Assess the background quality.
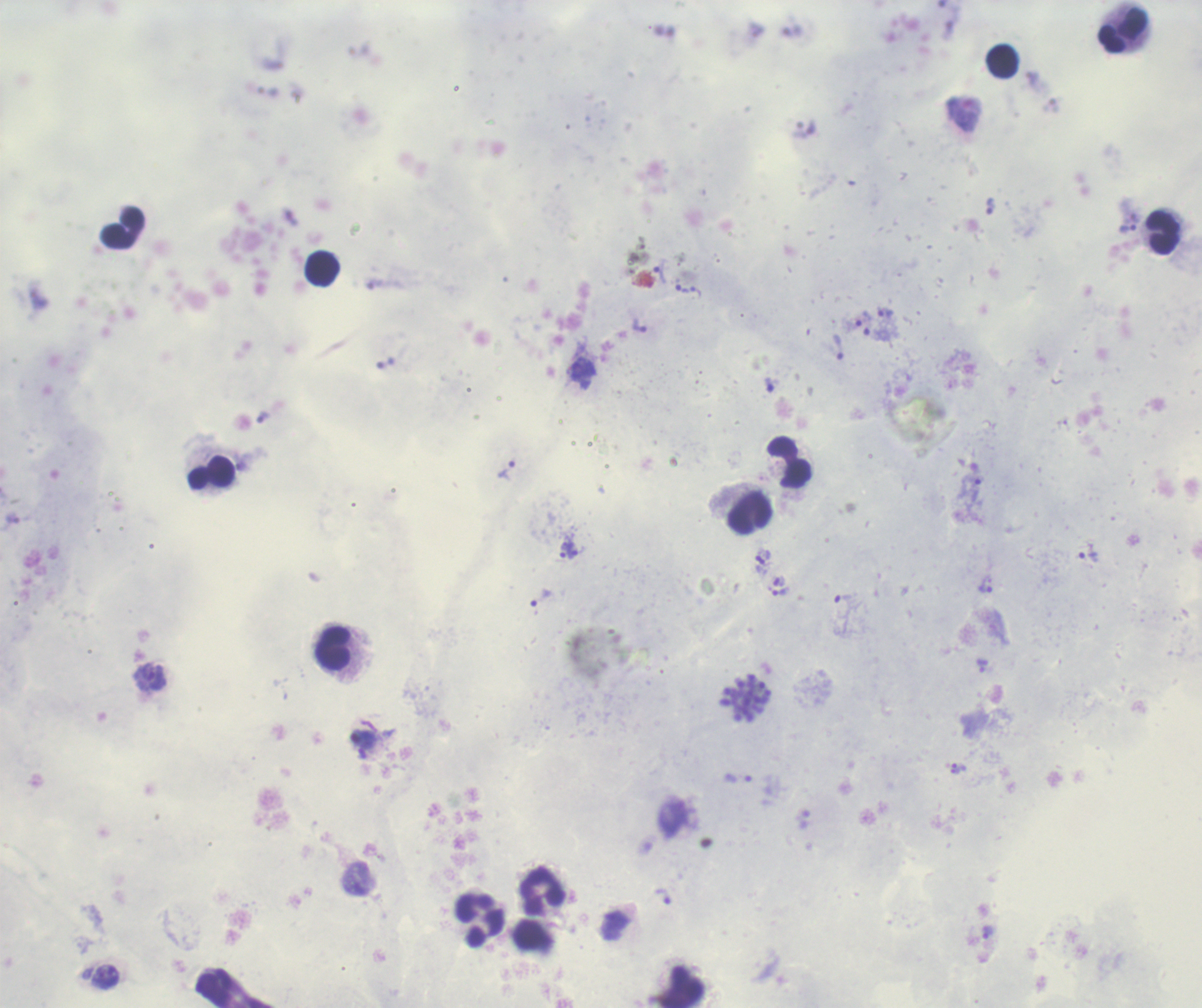
Good.

Approximate object centers, in pixels from the top-left corner. Leukocyte locations: (x=1123, y=32), (x=1002, y=60), (x=122, y=228), (x=1161, y=232), (x=321, y=269), (x=789, y=463), (x=212, y=472), (x=750, y=513), (x=333, y=648), (x=542, y=892), (x=482, y=920), (x=682, y=987). Trophozoite locations: (x=963, y=114), (x=989, y=205), (x=1128, y=229), (x=659, y=271), (x=681, y=289), (x=696, y=293), (x=884, y=311), (x=863, y=318), (x=639, y=326), (x=877, y=334), (x=838, y=347), (x=506, y=469), (x=976, y=489), (x=567, y=551), (x=1087, y=556), (x=985, y=583), (x=777, y=590), (x=541, y=597), (x=843, y=597), (x=982, y=666), (x=150, y=677), (x=362, y=739), (x=958, y=769), (x=738, y=778), (x=662, y=897), (x=988, y=931). Schizont locations: (x=746, y=698). Life-cycle stages observed: trophozoite, schizont. Thick smear of blood. Single field of view. Previously used in a real diagnosis. Romanowsky stain. Coloration quality: good. Captured at 100x magnification. Image is 1202×1008 pixels. Result: malaria parasites identified.